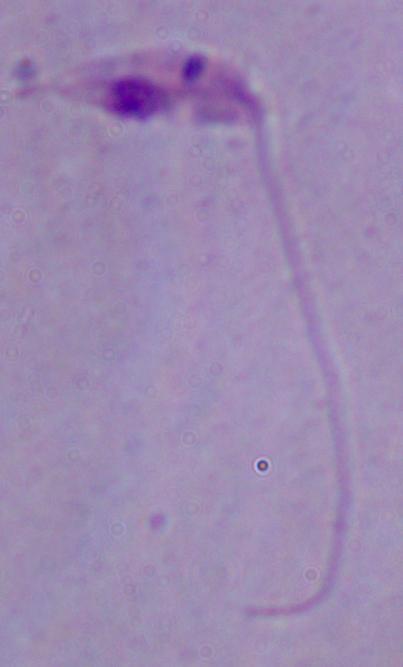

Summary:
  - Magnification: 1000x
  - Modality: photomicrograph
  - Identification: Leishmania